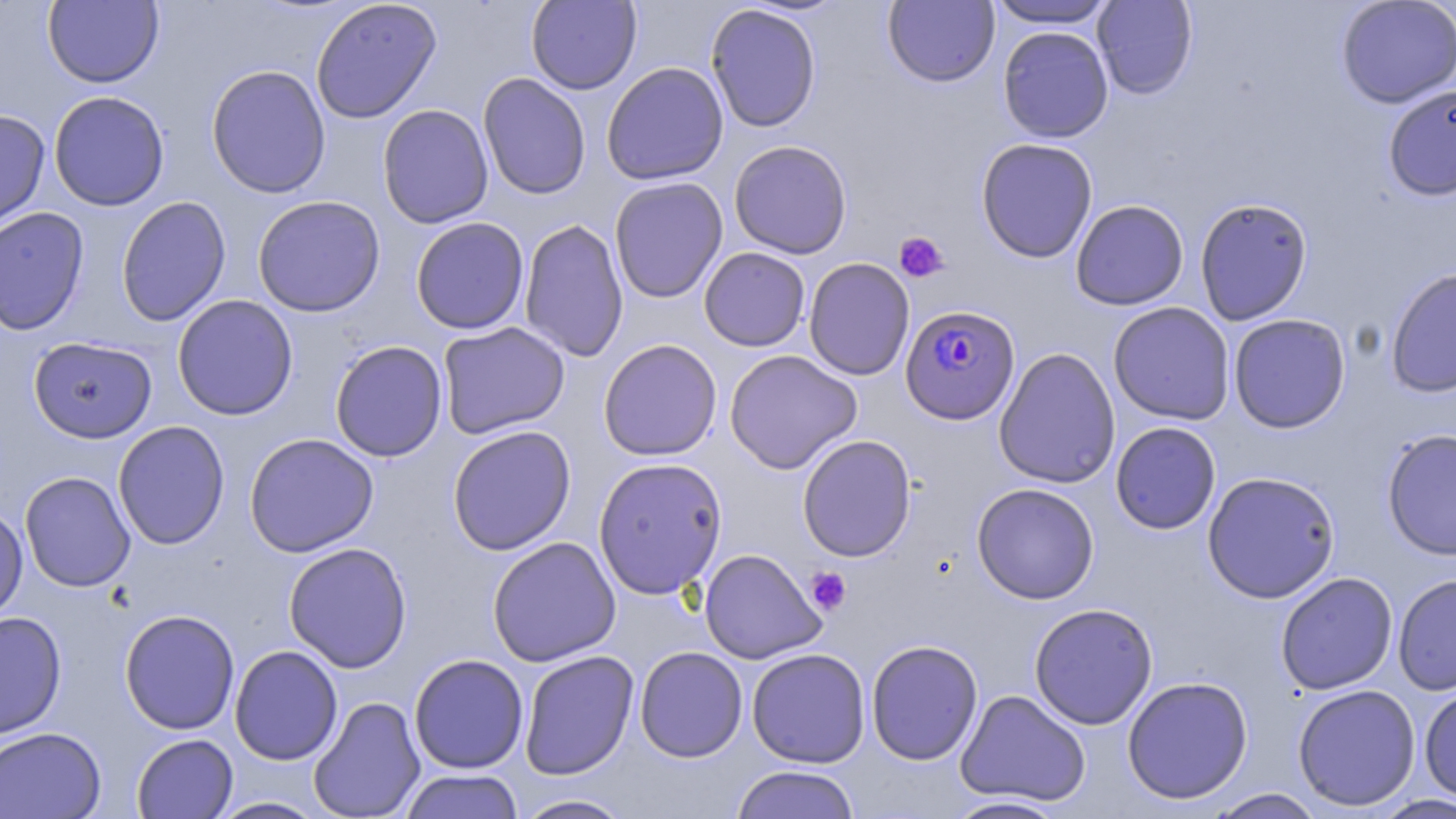

slide_level_diagnosis: Plasmodium falciparum
modality: optical microscopy
magnification: 1000x
field_of_view: single
preparation: thin blood smear
stain: May-Grünwald-Giemsa
plasmodium_falciparum_infected_red_blood_cell_locations: 'approximate bounding boxes as named x1/y1/x2/y2 corners in pixels: (x1=900, y1=304, x2=1021, y2=424)'
image_size: 1456×819 pixels
platelet_locations: 'approximate bounding boxes as named x1/y1/x2/y2 corners in pixels: (x1=894, y1=232, x2=949, y2=283), (x1=806, y1=568, x2=851, y2=616)'
uninfected_red_blood_cell_locations: 'approximate bounding boxes as named x1/y1/x2/y2 corners in pixels: (x1=42, y1=0, x2=164, y2=88), (x1=310, y1=0, x2=442, y2=124), (x1=527, y1=0, x2=642, y2=95), (x1=883, y1=0, x2=1000, y2=87), (x1=1092, y1=0, x2=1198, y2=100), (x1=1336, y1=0, x2=1455, y2=108), (x1=985, y1=1, x2=1121, y2=29), (x1=705, y1=4, x2=822, y2=133), (x1=997, y1=25, x2=1114, y2=143), (x1=601, y1=61, x2=729, y2=185), (x1=206, y1=64, x2=331, y2=198), (x1=478, y1=72, x2=591, y2=200), (x1=1382, y1=84, x2=1456, y2=201), (x1=48, y1=90, x2=170, y2=211), (x1=377, y1=104, x2=494, y2=228), (x1=0, y1=108, x2=50, y2=231), (x1=976, y1=137, x2=1098, y2=263), (x1=728, y1=140, x2=853, y2=259), (x1=609, y1=176, x2=728, y2=303), (x1=116, y1=195, x2=231, y2=327), (x1=251, y1=195, x2=386, y2=317), (x1=1195, y1=197, x2=1312, y2=325), (x1=1070, y1=199, x2=1188, y2=310), (x1=0, y1=206, x2=89, y2=335), (x1=410, y1=216, x2=529, y2=334), (x1=519, y1=218, x2=629, y2=362), (x1=699, y1=247, x2=810, y2=352), (x1=803, y1=257, x2=915, y2=381), (x1=1385, y1=267, x2=1456, y2=398), (x1=172, y1=294, x2=298, y2=421), (x1=1108, y1=302, x2=1235, y2=425), (x1=1228, y1=313, x2=1351, y2=433), (x1=437, y1=321, x2=570, y2=439), (x1=28, y1=336, x2=157, y2=443), (x1=598, y1=339, x2=723, y2=461), (x1=329, y1=340, x2=448, y2=462), (x1=994, y1=347, x2=1121, y2=489), (x1=724, y1=349, x2=862, y2=473), (x1=113, y1=421, x2=230, y2=550), (x1=1110, y1=421, x2=1221, y2=535), (x1=447, y1=425, x2=577, y2=556), (x1=1381, y1=429, x2=1456, y2=560), (x1=244, y1=432, x2=379, y2=558), (x1=797, y1=434, x2=917, y2=562), (x1=593, y1=457, x2=728, y2=599), (x1=20, y1=471, x2=136, y2=592), (x1=1202, y1=471, x2=1341, y2=603), (x1=971, y1=482, x2=1100, y2=604), (x1=0, y1=503, x2=29, y2=625), (x1=487, y1=536, x2=621, y2=667), (x1=283, y1=542, x2=413, y2=673), (x1=699, y1=548, x2=827, y2=664), (x1=1275, y1=572, x2=1398, y2=695), (x1=1392, y1=573, x2=1456, y2=696), (x1=1029, y1=603, x2=1158, y2=730), (x1=119, y1=609, x2=240, y2=734), (x1=0, y1=611, x2=67, y2=740), (x1=865, y1=639, x2=983, y2=765), (x1=229, y1=645, x2=343, y2=766), (x1=634, y1=646, x2=748, y2=762), (x1=746, y1=647, x2=871, y2=768), (x1=518, y1=650, x2=639, y2=780), (x1=409, y1=653, x2=529, y2=773), (x1=1121, y1=675, x2=1254, y2=804), (x1=1292, y1=683, x2=1421, y2=811), (x1=1418, y1=684, x2=1456, y2=803), (x1=955, y1=689, x2=1091, y2=807), (x1=308, y1=695, x2=426, y2=819), (x1=0, y1=727, x2=106, y2=818), (x1=131, y1=733, x2=238, y2=819), (x1=730, y1=765, x2=861, y2=819), (x1=399, y1=769, x2=524, y2=819), (x1=1205, y1=788, x2=1327, y2=818), (x1=1372, y1=793, x2=1456, y2=818), (x1=511, y1=794, x2=636, y2=819), (x1=942, y1=795, x2=1070, y2=818), (x1=206, y1=797, x2=330, y2=818)'